Assess the background quality.
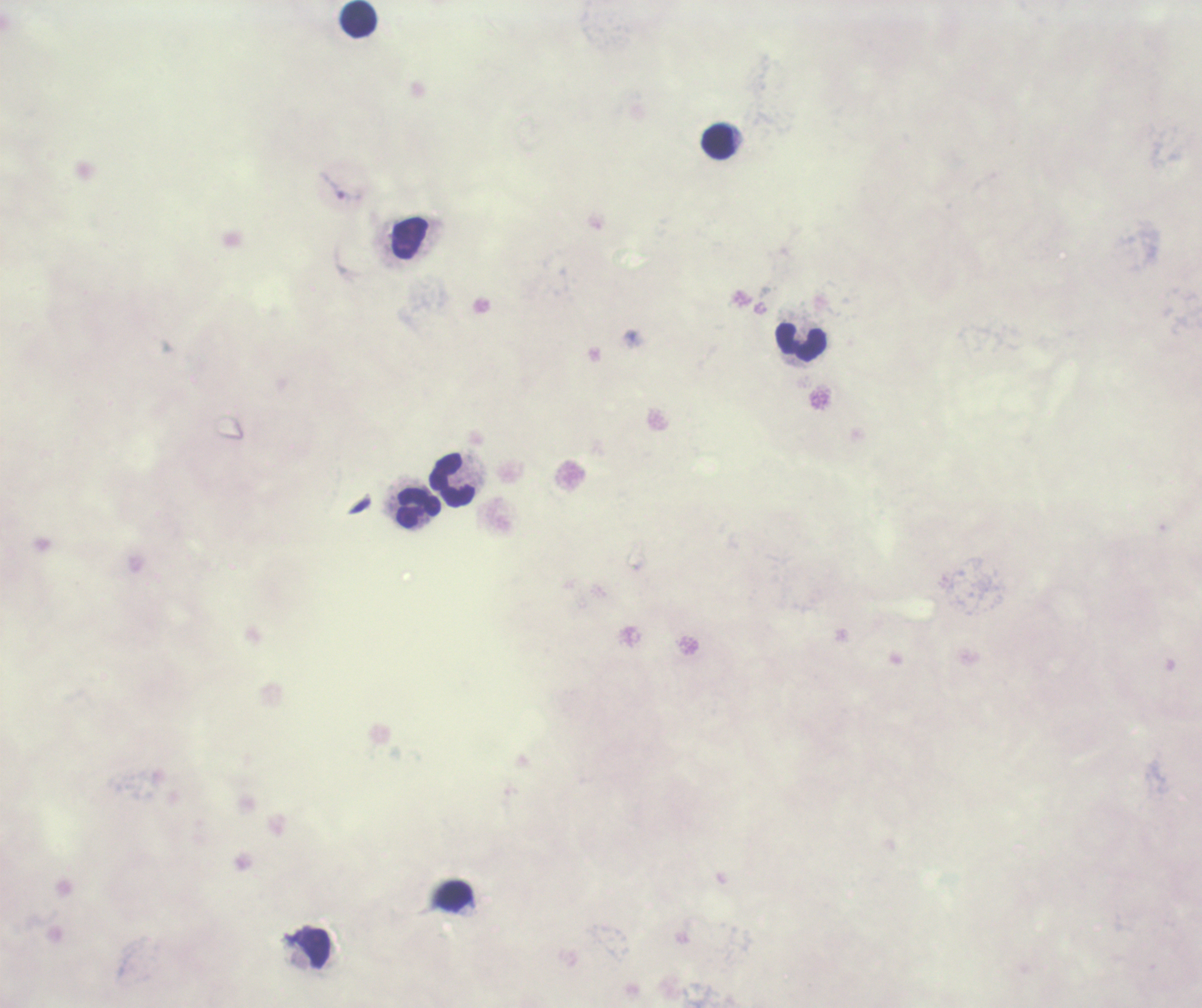
It is poor.

Approximate centers as (x, y) in pixels.
Summary:
  - Leukocyte locations: (359, 19), (719, 142), (801, 343), (452, 480), (419, 508), (315, 949)
  - Trophozoite locations: (333, 185)
  - Result: Plasmodium parasites identified
  - Context: previously used in an actual diagnosis
  - Image size: 1202×1008 pixels
  - Stain: Romanowsky
  - Preparation: thick blood smear
  - Magnification: 100x
  - Coloration quality: bad
  - Field of view: single